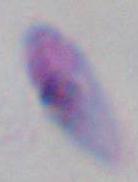

Toxoplasma gondii is seen. Photomicrograph. Captured at 1000x magnification.